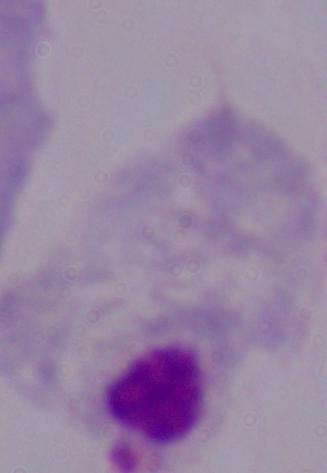
1000x magnification. Photomicrograph. A trichomonad is seen.